Locate every blood parasite and identify its species.
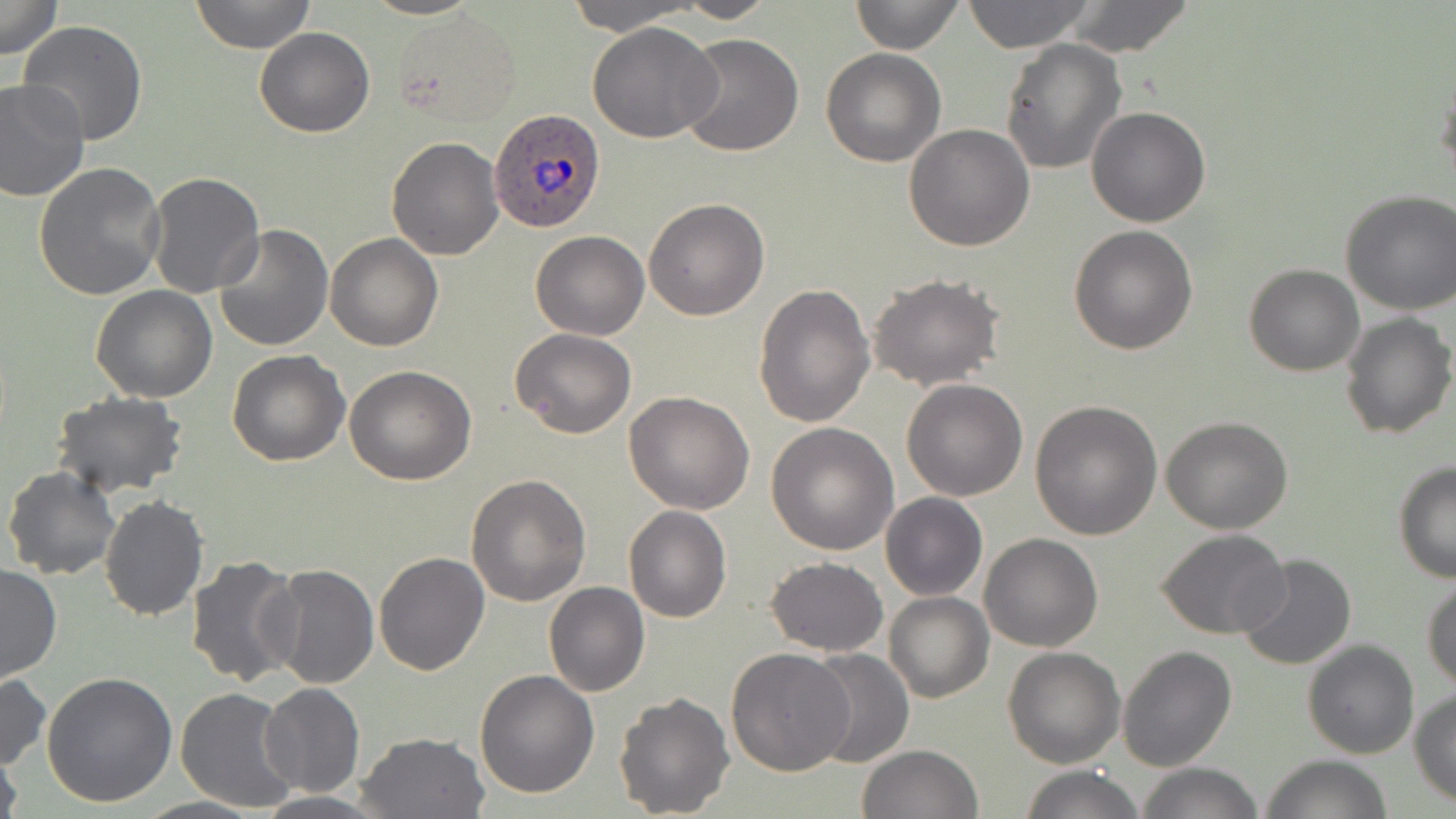

Approximate bounding boxes as (x1, y1, x2, y2) in pixels.
Plasmodium ovale-infected red blood cells: (488, 109, 609, 233).
No Plasmodium falciparum, Plasmodium malariae, Plasmodium vivax, Babesia divergens, or Trypanosoma brucei observed.

Summary:
  - Uninfected red blood cell locations: (0, 0, 63, 59), (189, 0, 317, 53), (363, 0, 481, 20), (564, 0, 700, 33), (666, 0, 779, 23), (851, 0, 964, 54), (960, 0, 1095, 52), (1060, 1, 1197, 57), (392, 10, 521, 127), (17, 20, 150, 147), (587, 21, 722, 142), (255, 27, 375, 137), (677, 33, 804, 157), (1001, 37, 1128, 176), (820, 47, 945, 167), (1434, 67, 1456, 187), (0, 79, 91, 204), (1086, 106, 1212, 227), (903, 123, 1034, 251), (386, 137, 504, 260), (33, 163, 167, 303), (145, 171, 266, 298), (1336, 191, 1456, 315), (642, 198, 768, 321), (214, 223, 334, 353), (1069, 225, 1199, 355), (531, 231, 649, 339), (325, 233, 444, 351), (1244, 264, 1365, 376), (867, 272, 1005, 390), (752, 282, 875, 429), (91, 285, 218, 402), (1340, 311, 1455, 440), (509, 328, 637, 439), (226, 348, 349, 466), (344, 364, 476, 484), (901, 378, 1029, 501), (50, 390, 188, 496), (623, 390, 756, 514), (1030, 400, 1163, 541), (1161, 417, 1293, 535), (765, 422, 899, 555), (1393, 461, 1456, 584), (3, 467, 121, 581), (466, 473, 592, 608), (880, 493, 987, 600), (99, 497, 209, 621), (623, 504, 732, 622), (1156, 529, 1291, 639), (979, 533, 1103, 651), (373, 553, 490, 675), (184, 554, 304, 688), (1236, 554, 1357, 672), (765, 557, 887, 654), (264, 562, 379, 688), (0, 564, 61, 683), (1422, 577, 1456, 692), (543, 582, 650, 697), (884, 591, 994, 703), (1300, 638, 1419, 759), (1117, 644, 1237, 771), (803, 646, 914, 769), (726, 647, 855, 776), (1002, 647, 1125, 769), (474, 668, 600, 798), (42, 672, 178, 808), (0, 674, 51, 771), (259, 683, 364, 796), (175, 686, 299, 814), (1410, 689, 1456, 806), (614, 691, 734, 819), (355, 731, 490, 818), (0, 744, 24, 819), (856, 744, 982, 819), (1264, 754, 1391, 819), (1136, 763, 1264, 818), (1017, 766, 1143, 819), (252, 792, 388, 819)
  - Slide-level diagnosis: Plasmodium ovale
  - Preparation: thin blood smear
  - Field of view: single
  - Magnification: 1000x
  - Modality: light microscopy
  - Stain: May-Grünwald-Giemsa
  - Image size: 1456×819 pixels